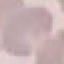

Summary:
  - Malaria status: uninfected
  - Preparation: thin smear
  - Image type: automatically extracted cell patch, resized to 64 × 64 pixels
  - Capture: smartphone through the microscope eyepiece
  - Stain: Giemsa